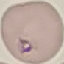
Result: malaria parasites detected. Thin blood smear. Acquired by smartphone through the microscope eyepiece. Giemsa stain. Cell patch, automatically extracted from a larger field of view and resized to 64 × 64 pixels.